Locate and identify every blood parasite.
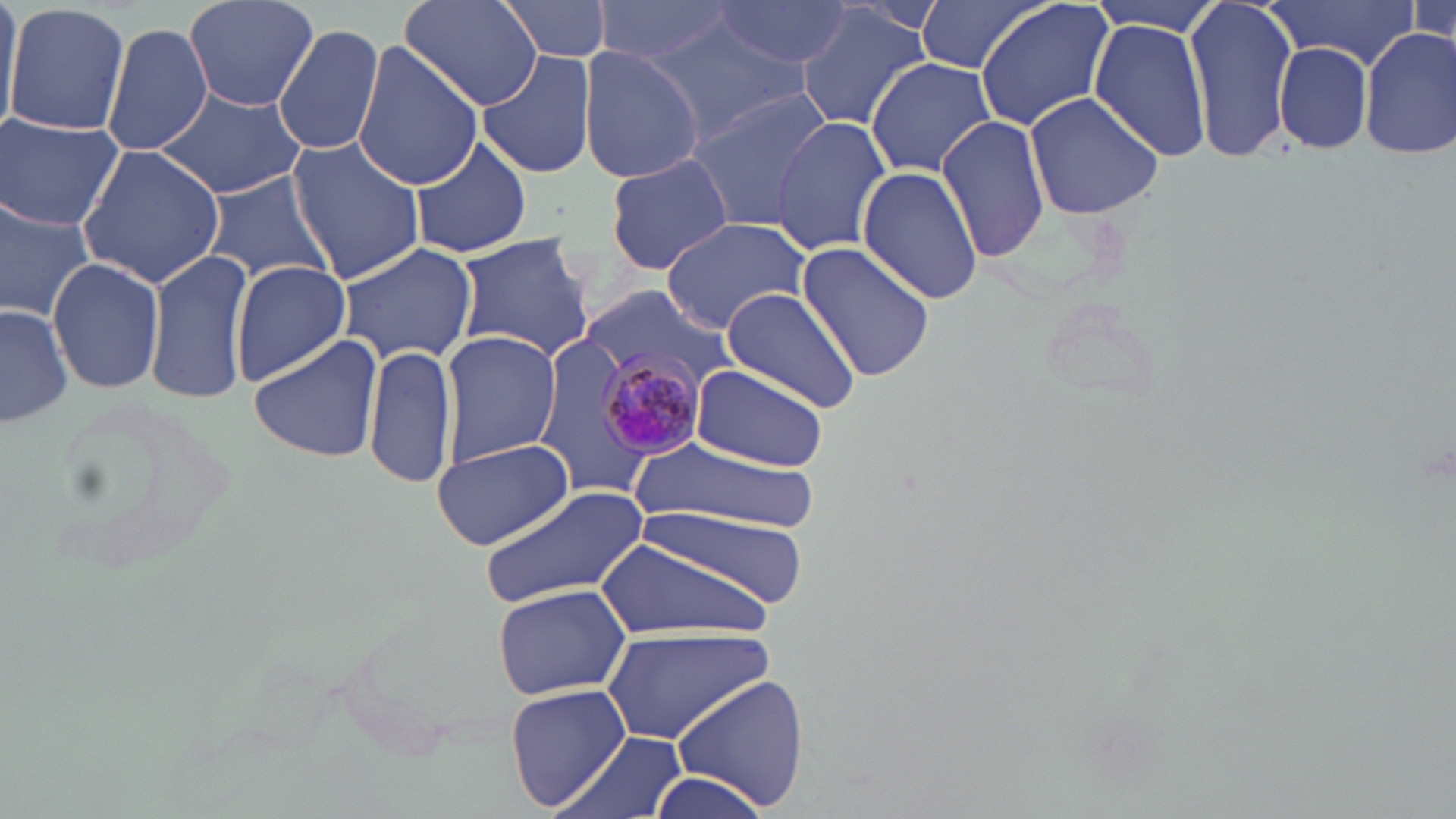
Approximate bounding boxes as (x1, y1, x2, y2) in pixels.
Plasmodium malariae-infected red blood cells: (591, 349, 706, 465).
No Plasmodium falciparum, Plasmodium ovale, Plasmodium vivax, Babesia divergens, or Trypanosoma brucei observed.

Uninfected red blood cell locations: (0, 0, 22, 130), (181, 0, 318, 114), (401, 0, 543, 112), (497, 0, 616, 66), (713, 0, 853, 68), (914, 0, 1051, 75), (974, 0, 1117, 130), (1184, 0, 1298, 166), (1261, 0, 1424, 67), (594, 1, 740, 67), (1084, 1, 1229, 33), (5, 3, 130, 137), (794, 8, 930, 130), (1088, 20, 1213, 162), (104, 24, 214, 156), (274, 24, 385, 157), (655, 27, 810, 139), (1359, 29, 1455, 162), (282, 31, 401, 265), (1273, 41, 1376, 156), (352, 43, 484, 188), (578, 46, 704, 184), (477, 51, 597, 179), (865, 58, 998, 176), (154, 82, 307, 200), (687, 89, 833, 232), (1023, 92, 1166, 219), (0, 112, 125, 232), (770, 115, 893, 253), (937, 115, 1053, 261), (286, 136, 427, 284), (404, 138, 534, 257), (78, 142, 227, 289), (605, 152, 734, 275), (856, 168, 986, 306), (204, 172, 333, 290), (0, 194, 97, 320), (659, 216, 812, 336), (451, 232, 596, 359), (794, 240, 938, 384), (337, 241, 480, 366), (145, 249, 254, 404), (47, 255, 165, 395), (232, 260, 352, 385), (577, 286, 742, 403), (720, 286, 863, 412), (0, 303, 73, 426), (439, 329, 560, 466), (248, 334, 387, 463), (534, 334, 643, 493), (364, 345, 455, 493), (690, 363, 831, 471), (37, 393, 243, 575), (428, 436, 575, 550), (633, 441, 814, 531), (484, 487, 651, 609), (605, 510, 801, 633), (491, 583, 630, 700), (601, 626, 778, 744), (667, 674, 809, 812), (505, 683, 633, 813), (554, 729, 689, 819), (644, 773, 775, 819). Slide-level diagnosis: Plasmodium malariae. Captured at 1000x magnification. Image is 1456×819 pixels. Light microscopy. Thin blood film. One field of a larger specimen. May-Grünwald-Giemsa stain.